Assess this cell for malaria.
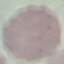

It is uninfected.

Thin blood smear. Giemsa-stained preparation. Photographed with a smartphone camera at the microscope eyepiece. Automatically extracted cell patch, resized to 64 × 64 pixels.